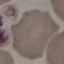
Result: negative for malaria parasites. Thin blood film. Giemsa stain. Cell patch, automatically extracted from a larger field of view and resized to 64 × 64 pixels. Photographed with a smartphone camera at the microscope eyepiece.